Locate every uninfected red blood cell.
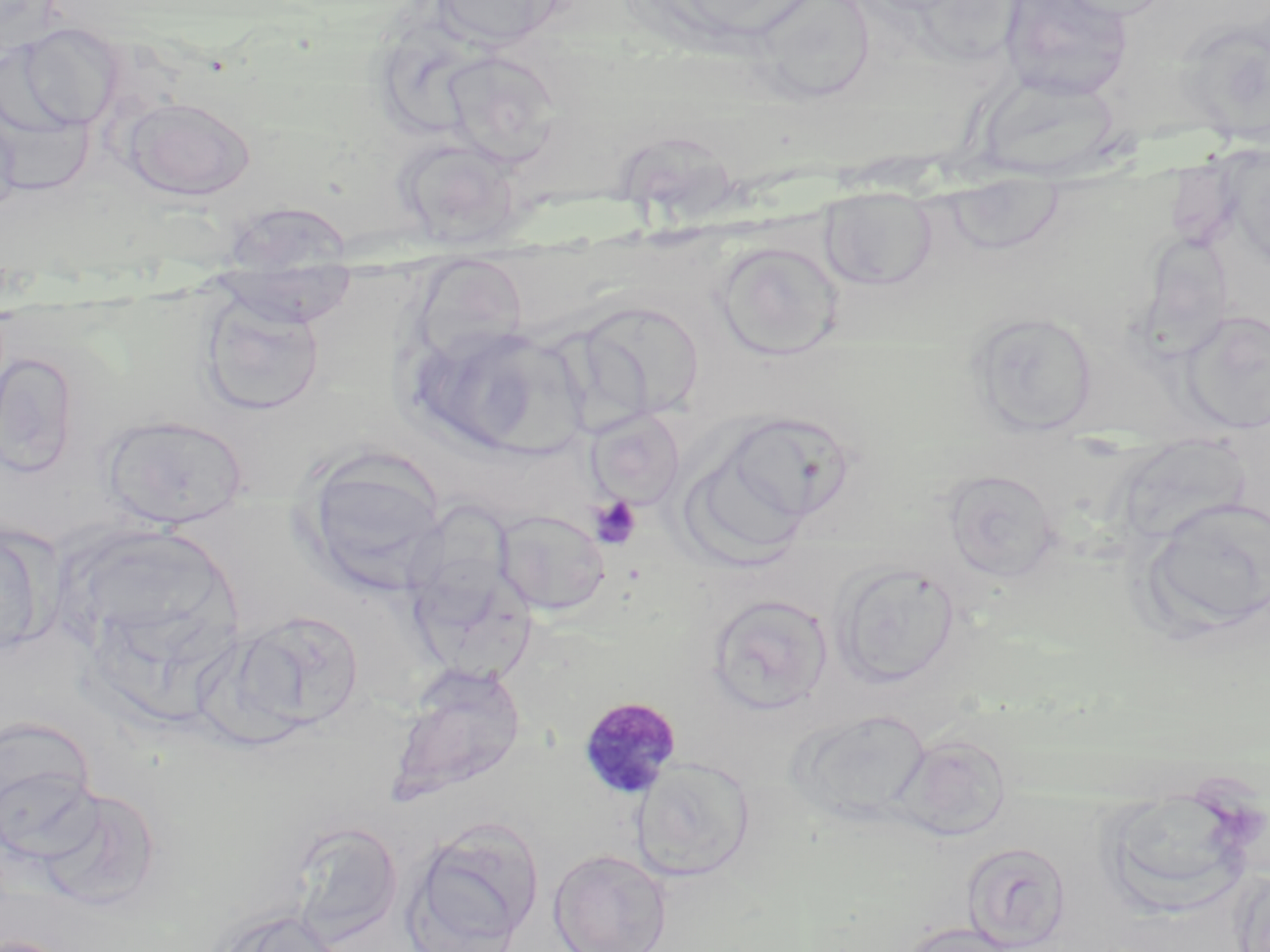
Approximate bounding boxes as named x1/y1/x2/y2 corners in pixels.
Uninfected red blood cells: (x1=430, y1=0, x2=568, y2=50), (x1=999, y1=0, x2=1134, y2=100), (x1=1047, y1=0, x2=1180, y2=21), (x1=749, y1=1, x2=878, y2=103), (x1=1176, y1=20, x2=1270, y2=145), (x1=6, y1=22, x2=124, y2=134), (x1=439, y1=49, x2=561, y2=167), (x1=978, y1=72, x2=1122, y2=182), (x1=0, y1=90, x2=97, y2=200), (x1=122, y1=96, x2=256, y2=201), (x1=0, y1=104, x2=21, y2=221), (x1=391, y1=136, x2=524, y2=249), (x1=1226, y1=143, x2=1269, y2=278), (x1=943, y1=173, x2=1066, y2=257), (x1=819, y1=185, x2=937, y2=291), (x1=216, y1=200, x2=356, y2=271), (x1=715, y1=241, x2=843, y2=358), (x1=409, y1=254, x2=531, y2=368), (x1=211, y1=267, x2=358, y2=328), (x1=199, y1=292, x2=325, y2=417), (x1=578, y1=300, x2=705, y2=420), (x1=967, y1=310, x2=1098, y2=436), (x1=1179, y1=310, x2=1270, y2=435), (x1=409, y1=323, x2=574, y2=455), (x1=1, y1=347, x2=81, y2=480), (x1=586, y1=409, x2=685, y2=509), (x1=716, y1=409, x2=861, y2=537), (x1=101, y1=414, x2=250, y2=530), (x1=679, y1=431, x2=817, y2=567), (x1=301, y1=452, x2=446, y2=593), (x1=942, y1=468, x2=1061, y2=583), (x1=1139, y1=496, x2=1270, y2=638), (x1=403, y1=497, x2=524, y2=630), (x1=494, y1=509, x2=611, y2=617), (x1=0, y1=522, x2=51, y2=660), (x1=61, y1=524, x2=244, y2=669), (x1=831, y1=562, x2=962, y2=689), (x1=411, y1=564, x2=544, y2=680), (x1=706, y1=593, x2=834, y2=715), (x1=225, y1=609, x2=366, y2=738), (x1=386, y1=663, x2=527, y2=806), (x1=790, y1=707, x2=930, y2=826), (x1=0, y1=717, x2=100, y2=864), (x1=894, y1=733, x2=1013, y2=841), (x1=631, y1=757, x2=754, y2=882), (x1=1098, y1=782, x2=1264, y2=920), (x1=36, y1=785, x2=161, y2=909), (x1=406, y1=818, x2=544, y2=952), (x1=287, y1=820, x2=403, y2=946), (x1=961, y1=841, x2=1071, y2=951), (x1=549, y1=849, x2=672, y2=952), (x1=1230, y1=866, x2=1270, y2=952), (x1=207, y1=905, x2=345, y2=952), (x1=895, y1=922, x2=1021, y2=952).

Platelet locations: (x1=589, y1=496, x2=642, y2=550). Plasmodium malariae-infected red blood cell locations: (x1=577, y1=695, x2=683, y2=800). Slide-level diagnosis: Plasmodium malariae. Optical microscopy. 1000x magnification. Image is 1270×952 pixels. Thin blood smear. May-Grünwald-Giemsa-stained preparation. One field of a larger specimen.